Outline each Plasmodium parasite.
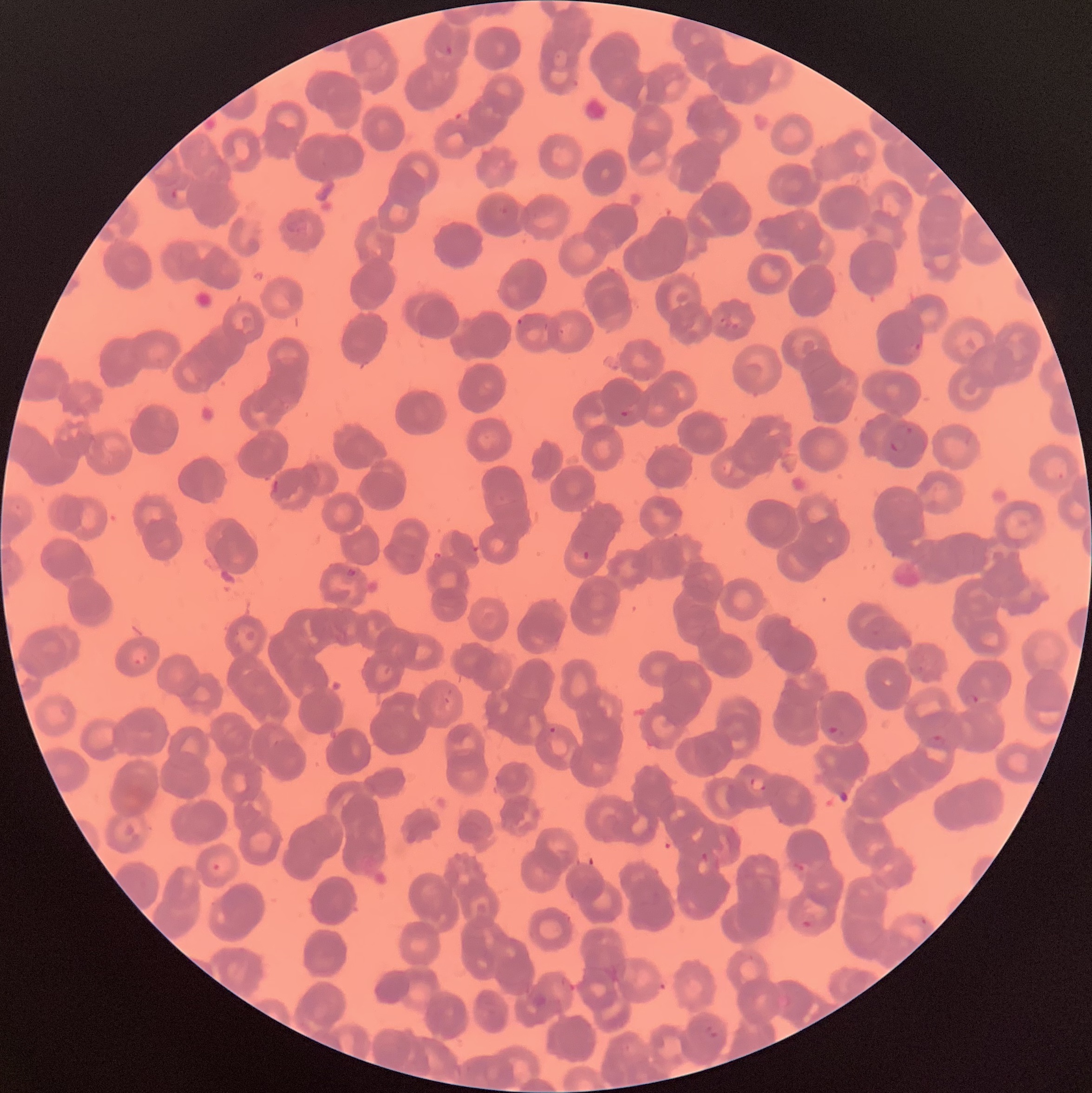

Approximate bounding boxes as (x1,y1)-(x2,y2) corner pairs in pixels.
Plasmodium parasites: (444,45)-(454,57), (170,188)-(179,200), (516,317)-(524,327), (914,342)-(921,353), (620,409)-(635,424), (905,426)-(914,436), (889,438)-(899,455), (582,549)-(591,561), (344,566)-(358,578), (964,692)-(980,708), (826,725)-(843,740), (549,726)-(558,735), (927,734)-(946,749), (748,777)-(766,792), (700,850)-(710,863), (211,862)-(221,871), (801,918)-(813,930), (704,1023)-(718,1040).

Thin blood smear. Optical microscopy. Image is 1092×1093 pixels. The red blood cells show rouleaux formation.